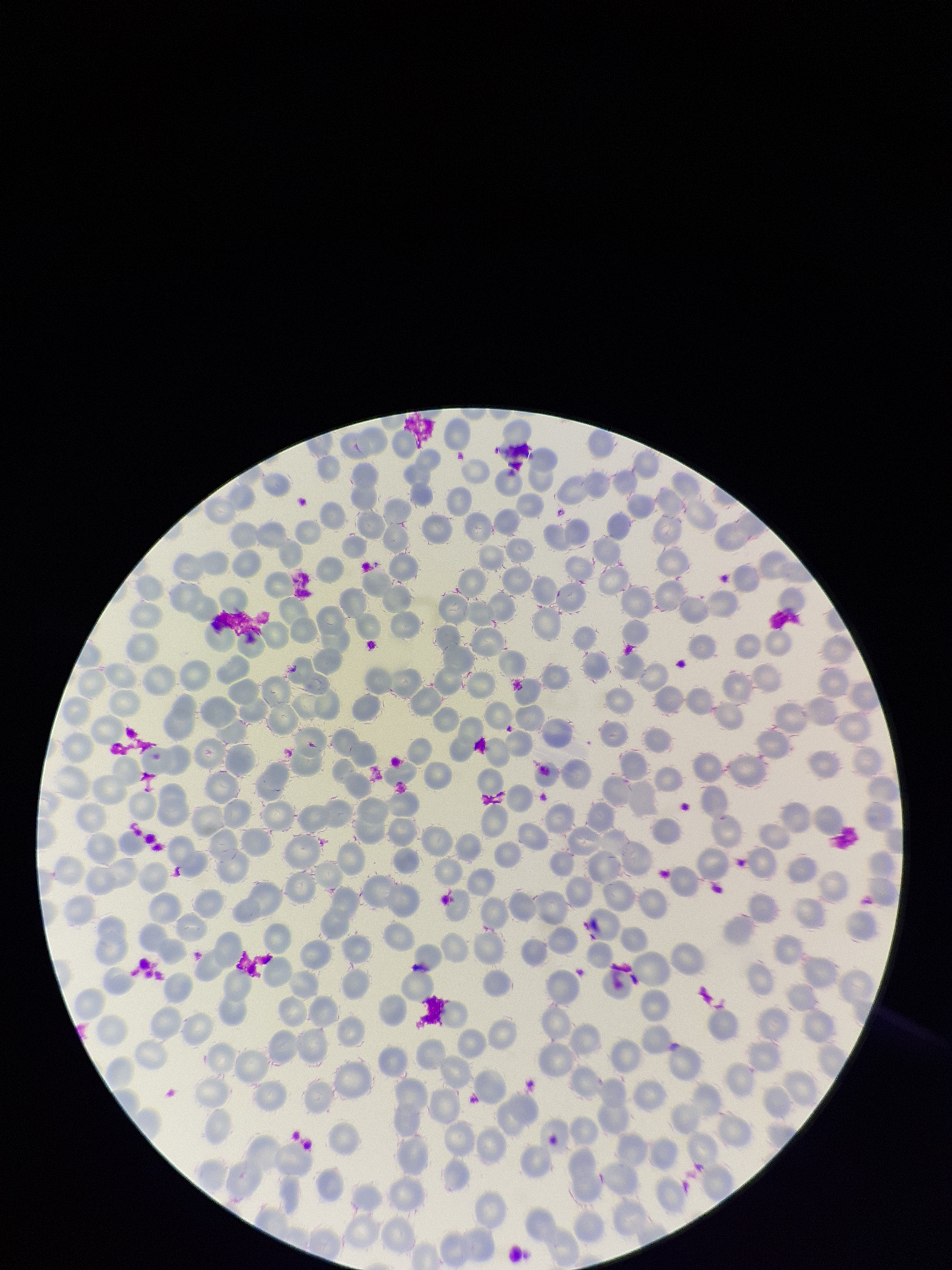 Photographed through the microscope eyepiece with a smartphone camera. Red blood cell count: 275. Image is 952×1270 pixels. Parasitized red blood cells: none seen. One field from this slide. Parasitized red blood cell count: 0. Preparation: thin blood smear. Patient malaria status: negative. Stained with Giemsa.